Assess this cell for malaria.
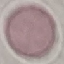

It is uninfected.

Summary:
  - Capture: smartphone through the microscope eyepiece
  - Stain: Giemsa
  - Image type: cell patch, automatically extracted from a larger field of view and resized to 64 × 64 pixels
  - Preparation: thin blood film